Give the extent of all Plasmodium vivax-infected red blood cells.
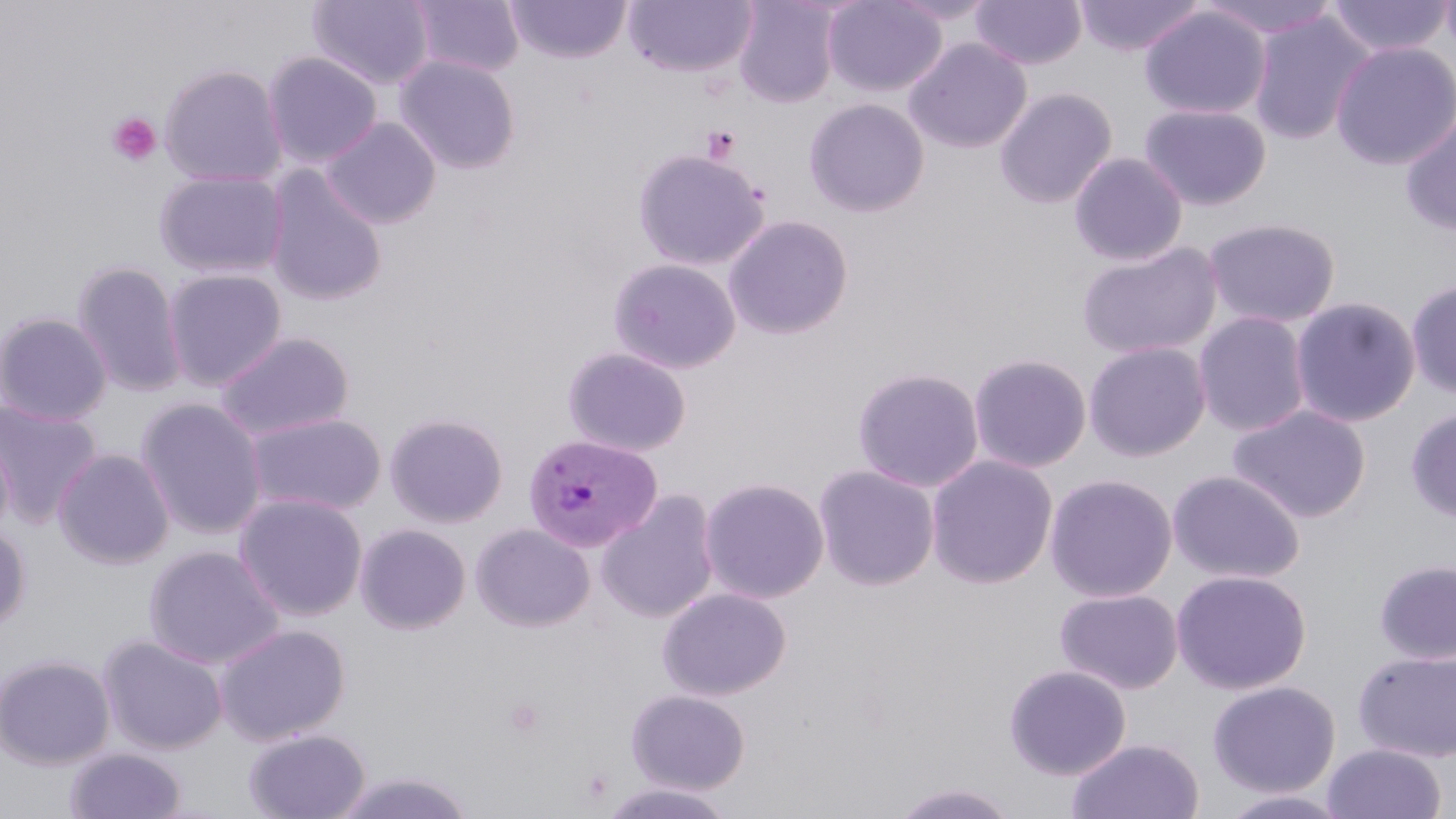
Approximate bounding boxes as (x1,y1)-(x2,y2) corner pairs in pixels.
Plasmodium vivax-infected red blood cells: (523,433)-(662,552).

Summary:
  - Platelet locations: (107,111)-(161,166), (702,126)-(741,164), (504,697)-(545,737)
  - Uninfected red blood cell locations: (307,0)-(435,89), (409,0)-(524,77), (507,0)-(631,64), (624,0)-(756,78), (732,0)-(841,107), (823,0)-(947,97), (969,0)-(1088,69), (1074,0)-(1206,57), (1198,0)-(1343,40), (1438,0)-(1456,57), (1326,1)-(1454,59), (1139,5)-(1271,120), (1248,11)-(1375,145), (903,36)-(1032,154), (1331,40)-(1456,170), (262,51)-(383,168), (393,54)-(522,175), (159,63)-(288,187), (994,86)-(1118,208), (804,97)-(930,217), (1138,103)-(1272,211), (1400,112)-(1456,236), (321,116)-(442,229), (632,148)-(768,271), (1069,151)-(1188,266), (264,167)-(388,307), (153,168)-(288,279), (723,214)-(854,339), (1202,217)-(1341,328), (1076,241)-(1223,360), (607,257)-(742,374), (72,260)-(188,398), (162,268)-(287,390), (1406,280)-(1456,399), (1289,296)-(1421,428), (0,311)-(113,426), (1193,311)-(1311,436), (214,332)-(356,441), (1083,341)-(1212,462), (562,346)-(692,457), (968,352)-(1092,473), (852,367)-(985,492), (135,398)-(268,539), (0,400)-(103,528), (1227,404)-(1371,523), (1405,407)-(1456,522), (245,411)-(387,516), (384,411)-(509,528), (0,422)-(15,542), (53,448)-(175,569), (926,454)-(1058,589), (813,463)-(940,591), (1167,470)-(1306,584), (1044,473)-(1178,602), (698,476)-(830,603), (597,489)-(721,624), (234,492)-(368,621), (0,521)-(31,632), (354,523)-(472,634), (470,523)-(596,632), (143,545)-(285,669), (1374,559)-(1456,665), (1171,569)-(1311,694), (657,586)-(792,700), (1054,588)-(1183,694), (213,623)-(351,745), (98,634)-(228,755), (1353,648)-(1456,763), (0,654)-(116,770), (1004,664)-(1132,780), (1207,680)-(1341,798), (625,689)-(751,795), (243,727)-(372,819), (1066,737)-(1204,819), (1322,743)-(1447,818), (65,747)-(186,818), (331,770)-(477,818), (890,781)-(1019,818), (598,782)-(737,819), (1218,789)-(1352,818)
  - Slide-level diagnosis: Plasmodium vivax
  - Image size: 1456×819 pixels
  - Field of view: single
  - Preparation: thin blood film
  - Modality: optical microscopy
  - Stain: May-Grünwald-Giemsa
  - Magnification: 1000x